Locate and identify every blood parasite.
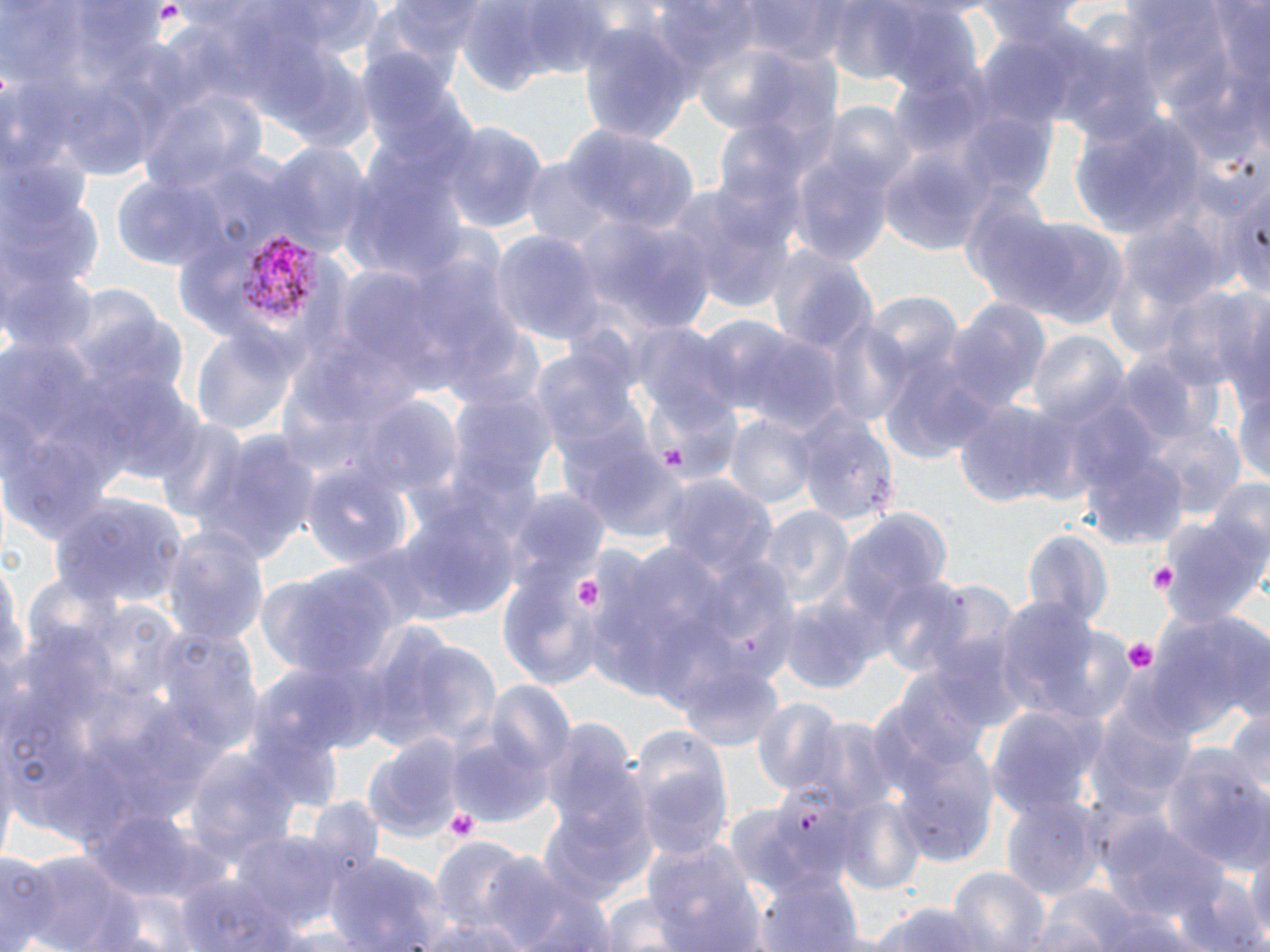
Approximate bounding boxes as (x1, y1, x2, y2) in pixels.
Plasmodium vivax-infected red blood cells: (236, 234, 324, 322).
No Plasmodium falciparum, Plasmodium ovale, Plasmodium malariae, Babesia divergens, or Trypanosoma brucei observed.

slide_level_diagnosis: Plasmodium vivax
preparation: thin blood smear
image_size: 1270×952 pixels
platelet_locations: 'approximate bounding boxes as (x1, y1, x2, y2) in pixels: (1148, 559, 1180, 596), (577, 578, 606, 608), (1123, 638, 1160, 674), (445, 806, 479, 842)'
modality: optical microscopy
magnification: 1000x
stain: May-Grünwald-Giemsa
field_of_view: one of a larger specimen
uninfected_red_blood_cell_locations: 'approximate bounding boxes as (x1, y1, x2, y2) in pixels: (739, 0, 861, 64), (463, 1, 621, 90), (657, 1, 761, 80), (842, 2, 987, 106), (576, 23, 697, 140), (138, 87, 263, 194), (1072, 116, 1209, 237), (439, 119, 547, 235), (564, 127, 697, 235), (787, 140, 897, 270), (259, 144, 371, 259), (876, 150, 990, 256), (111, 170, 234, 273), (667, 180, 794, 313), (3, 183, 103, 295), (1001, 215, 1132, 331), (598, 220, 721, 336), (490, 229, 604, 348), (765, 245, 876, 358), (3, 266, 100, 356), (1159, 289, 1267, 394), (862, 292, 963, 392), (944, 298, 1050, 413), (821, 319, 913, 428), (191, 326, 298, 439), (1026, 330, 1129, 428), (737, 332, 844, 433), (1114, 359, 1198, 447), (1233, 379, 1270, 491), (448, 394, 558, 510), (952, 399, 1069, 509), (356, 401, 462, 503), (797, 408, 898, 524), (724, 411, 820, 513), (155, 420, 250, 524), (1148, 421, 1245, 517), (190, 430, 323, 565), (566, 434, 689, 543), (1084, 447, 1191, 550), (298, 465, 413, 576), (660, 479, 778, 587), (509, 490, 611, 585), (51, 493, 186, 608), (401, 496, 521, 619), (838, 504, 949, 638), (756, 508, 854, 614), (1160, 510, 1270, 630), (161, 526, 270, 648), (1025, 529, 1113, 634), (0, 553, 27, 700), (255, 565, 392, 685), (497, 567, 609, 686), (874, 578, 978, 678), (780, 593, 885, 697), (994, 595, 1115, 725), (1151, 606, 1267, 737), (138, 620, 265, 756), (379, 633, 502, 753), (249, 662, 370, 765), (680, 664, 786, 752), (888, 674, 999, 776), (481, 683, 577, 788), (751, 698, 848, 799), (1088, 702, 1194, 809), (1226, 707, 1270, 799), (985, 709, 1105, 825), (631, 730, 734, 863), (363, 732, 466, 844), (448, 732, 558, 831), (174, 745, 300, 879), (1157, 747, 1268, 870), (894, 753, 998, 867), (835, 796, 926, 896), (1003, 797, 1101, 900), (538, 799, 653, 907), (93, 810, 202, 899), (1113, 822, 1227, 920), (235, 831, 356, 934), (432, 837, 531, 933), (1245, 839, 1269, 949), (643, 840, 768, 952), (488, 849, 609, 952), (0, 850, 55, 952), (19, 850, 145, 952), (324, 851, 445, 951), (948, 867, 1051, 952), (759, 869, 866, 952), (174, 873, 296, 952), (1173, 874, 1266, 952), (1036, 883, 1144, 950), (593, 893, 701, 951), (866, 901, 994, 952), (1090, 901, 1191, 952), (411, 912, 532, 952)'